Describe the morphology of the erythrocytes.
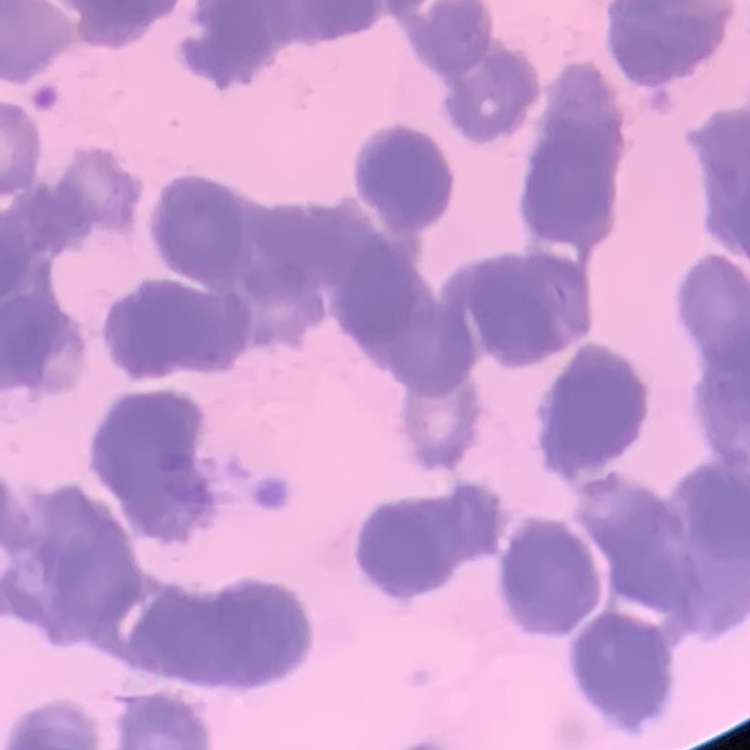

They show rouleaux formation.

preparation = thin peripheral smear
image type = one tile cut from a larger photomicrograph
stain = Field's or Giemsa